Classify this cell by malaria status.
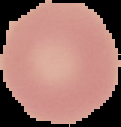

It is uninfected.

Summary:
  - Image size: 121×127 pixels
  - Image type: cell region segmented out of the field of view; surrounding area masked to black
  - Preparation: thin blood smear